State which parasite is depicted.
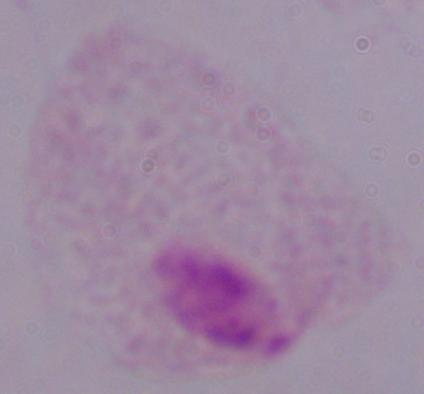

A trichomonad.

modality = photomicrograph
magnification = 1000x